Classify the preparation.
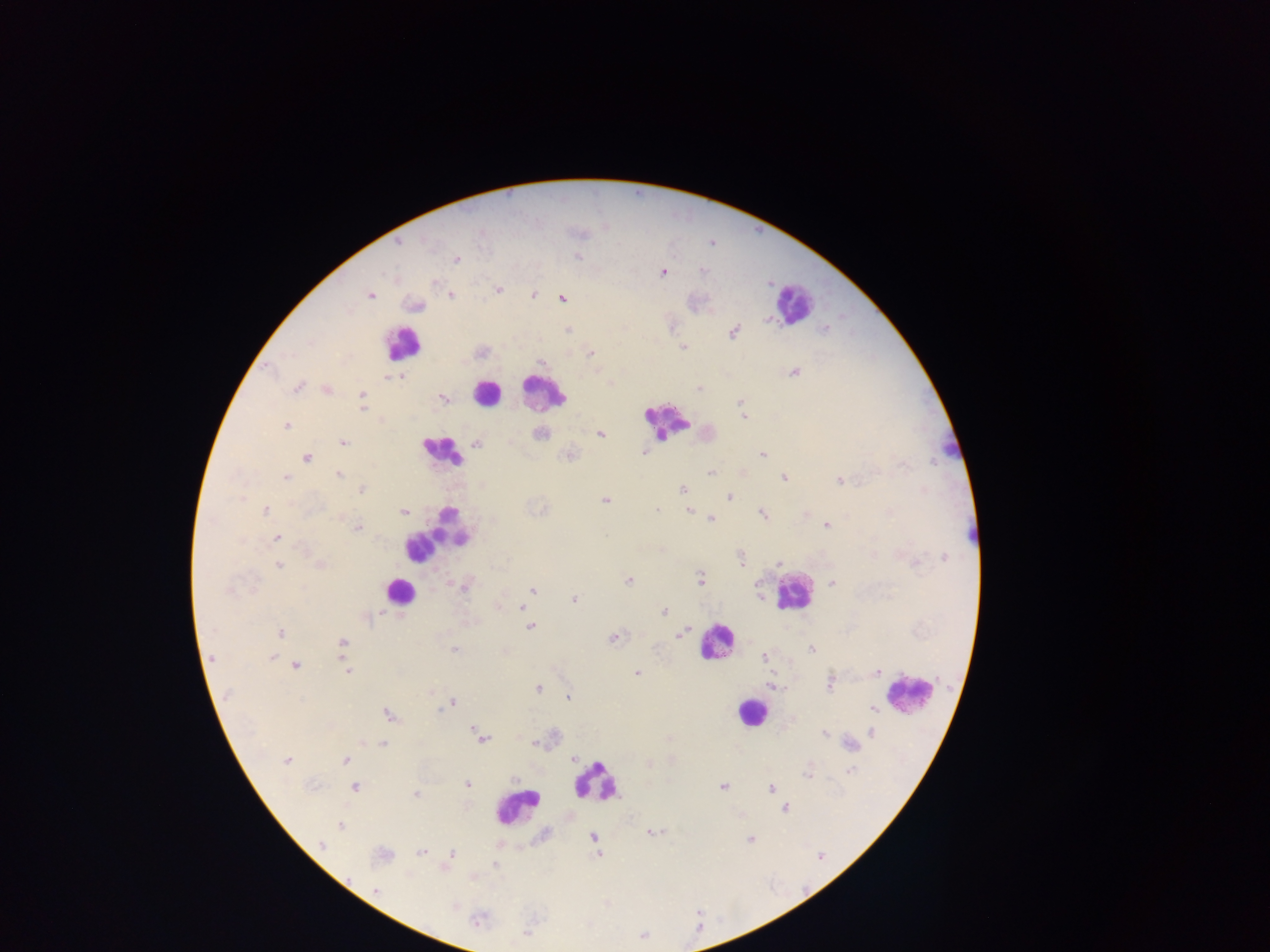

This is a thick smear.

Approximate centers as {x, y} in pixels.
Summary:
  - Plasmodium parasite locations: {396, 243}, {577, 257}, {456, 259}, {663, 272}, {434, 282}, {497, 290}, {369, 295}, {533, 295}, {449, 296}, {561, 298}, {414, 305}, {710, 311}, {826, 328}, {568, 330}, {733, 332}, {683, 346}, {590, 353}, {542, 362}, {793, 371}, {401, 376}, {297, 387}, {699, 388}, {326, 389}, {362, 394}, {443, 398}, {741, 401}, {362, 404}, {743, 416}, {286, 425}, {539, 433}, {600, 434}, {342, 443}, {476, 443}, {644, 452}, {762, 454}, {568, 455}, {305, 457}, {709, 472}, {741, 472}, {338, 474}, {285, 477}, {783, 478}, {838, 480}, {682, 488}, {361, 489}, {728, 497}, {605, 499}, {265, 510}, {403, 510}, {656, 510}, {688, 510}, {763, 514}, {805, 514}, {711, 518}, {826, 526}, {357, 528}, {276, 537}, {661, 550}, {944, 557}, {741, 560}, {779, 563}, {277, 565}, {320, 565}, {628, 580}, {699, 580}, {831, 582}, {465, 586}, {533, 589}, {760, 596}, {574, 599}, {521, 607}, {525, 612}, {663, 612}, {530, 626}, {280, 633}, {680, 634}, {614, 637}, {343, 644}, {812, 648}, {454, 650}, {272, 656}, {765, 657}, {211, 659}, {344, 664}, {296, 665}, {346, 671}, {877, 671}, {637, 673}, {829, 682}, {772, 685}, {537, 688}, {430, 692}, {568, 696}, {452, 702}, {873, 709}, {388, 715}, {471, 727}, {871, 731}, {824, 734}, {481, 738}, {362, 742}, {535, 742}, {382, 743}, {850, 744}, {573, 758}, {287, 760}, {345, 760}, {849, 770}, {807, 771}, {515, 778}, {467, 784}, {354, 787}, {723, 787}, {770, 788}, {415, 794}, {784, 807}, {339, 825}, {650, 832}, {592, 836}, {749, 838}, {320, 846}, {421, 852}, {381, 854}, {451, 854}, {598, 854}, {444, 867}, {376, 890}, {477, 920}, {526, 932}
  - Leukocyte locations: {793, 305}, {402, 343}, {543, 392}, {487, 393}, {666, 421}, {441, 451}, {437, 534}, {399, 591}, {793, 593}, {717, 642}, {908, 693}, {752, 711}, {595, 782}, {514, 805}
  - Country: Ghana
  - Capture: mobile-phone photograph through a microscope
  - Field of view: single
  - Image size: 1270×952 pixels